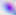
{
  "magnification": "400x",
  "identification": "Toxoplasma gondii",
  "modality": "photomicrograph"
}